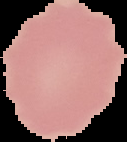

Summary:
  - Image type: segmented cell region on a black background
  - Result: negative for Plasmodium parasites
  - Image size: 127×142 pixels
  - Preparation: thin blood smear